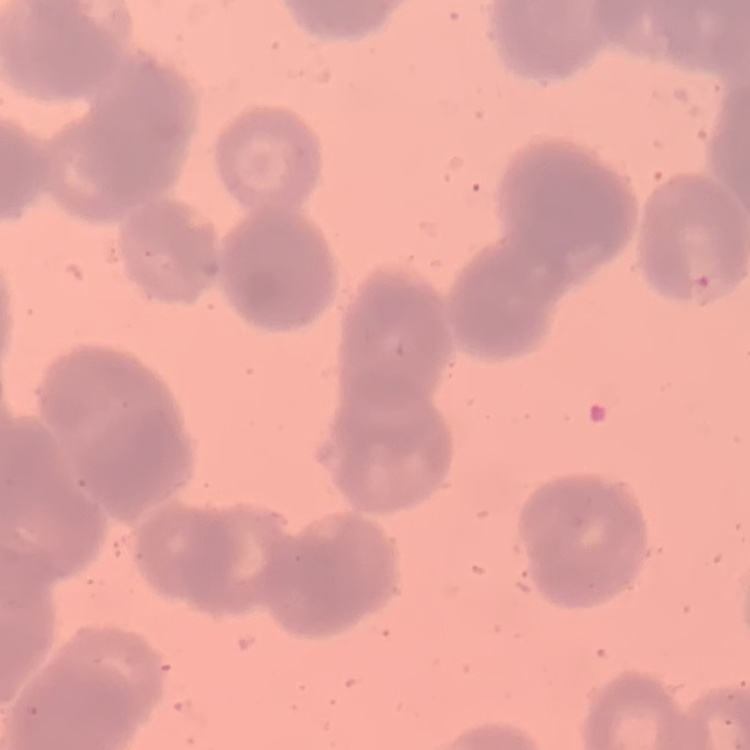

Summary:
  - Erythrocyte morphology: rouleaux formation
  - Stain: Field's or Giemsa
  - Preparation: thin blood film
  - Image type: one tile cut from a larger photomicrograph